Comment on the morphology of the erythrocytes.
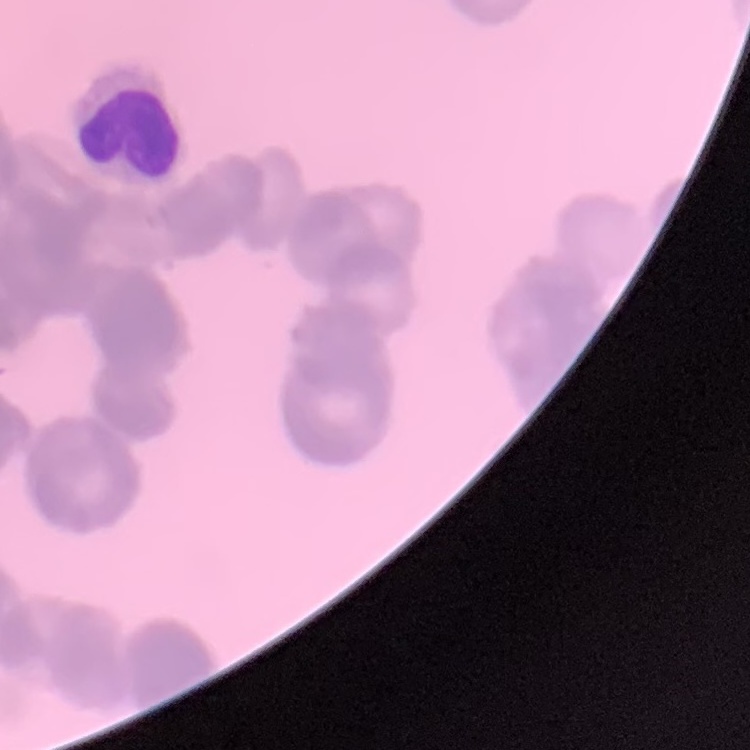
Rouleaux formation.

Field's or Giemsa stain. Thin peripheral smear. One tile cut from a larger photomicrograph.